Outline each blood parasite and name the species.
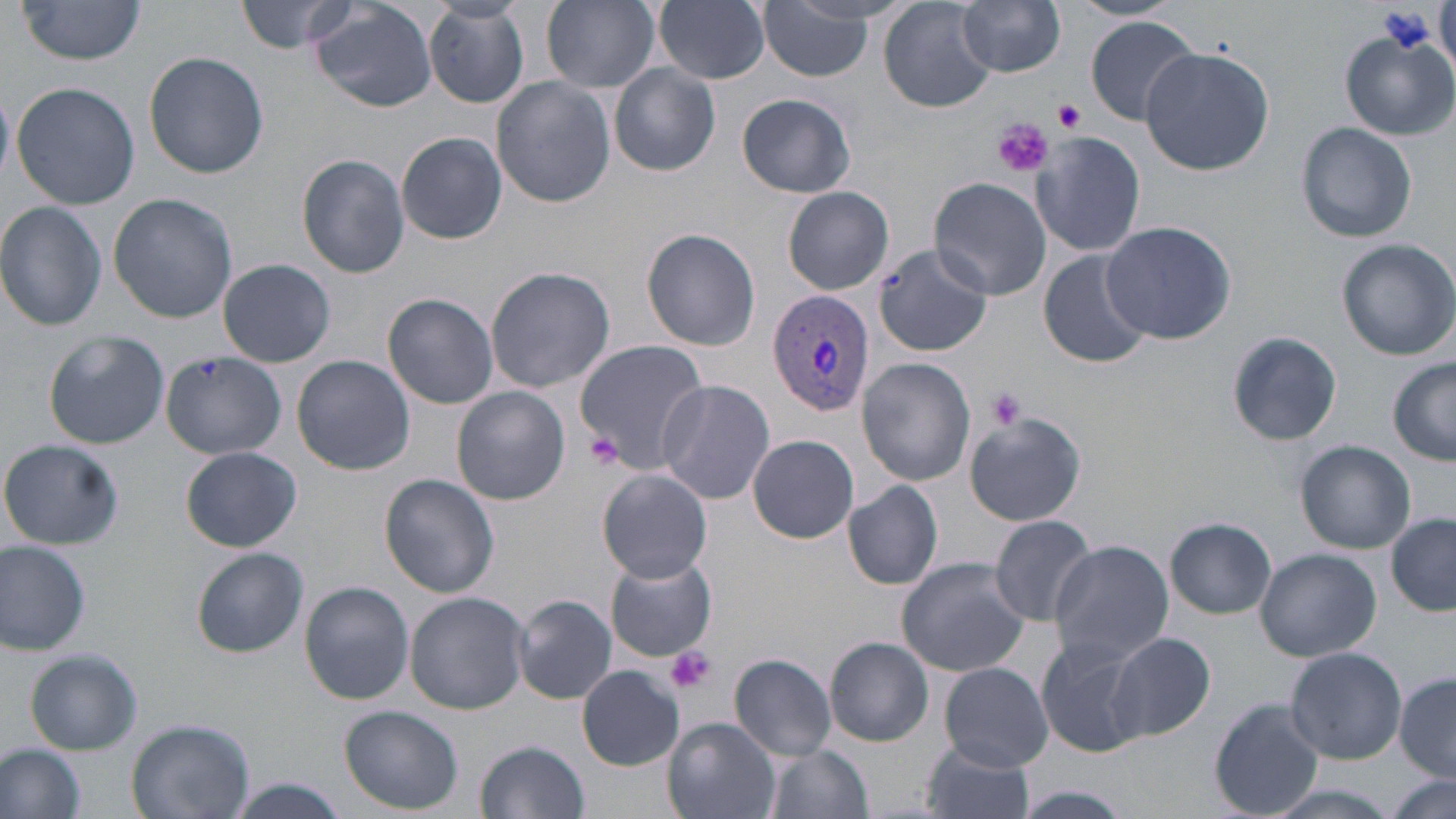

Approximate bounding boxes as [x1, y1, x2, y2] in pixels.
Plasmodium vivax-infected red blood cells: [768, 289, 875, 419].
No Plasmodium falciparum, Plasmodium ovale, Plasmodium malariae, Babesia divergens, or Trypanosoma brucei observed.

Platelet locations: [1054, 98, 1086, 132], [992, 118, 1052, 177], [985, 386, 1027, 429], [582, 432, 626, 468], [665, 646, 714, 694]. Uninfected red blood cell locations: [237, 0, 357, 54], [541, 0, 661, 91], [654, 0, 770, 85], [755, 0, 879, 82], [880, 0, 994, 113], [17, 1, 148, 67], [1069, 1, 1180, 22], [309, 2, 439, 112], [424, 2, 530, 110], [956, 2, 1066, 76], [1085, 16, 1201, 124], [1341, 33, 1456, 139], [1140, 44, 1277, 176], [144, 51, 269, 178], [608, 63, 721, 176], [491, 77, 618, 209], [12, 82, 141, 210], [737, 93, 856, 197], [1296, 121, 1417, 244], [396, 131, 507, 244], [1030, 131, 1146, 257], [296, 153, 410, 278], [929, 176, 1052, 301], [783, 186, 895, 294], [108, 192, 238, 322], [0, 201, 107, 331], [1100, 220, 1239, 345], [641, 228, 762, 351], [1336, 239, 1456, 360], [876, 241, 988, 356], [1037, 249, 1155, 369], [218, 258, 335, 368], [485, 266, 615, 394], [383, 293, 499, 409], [42, 329, 170, 450], [1225, 329, 1342, 446], [574, 339, 709, 467], [161, 349, 289, 460], [292, 355, 415, 476], [858, 358, 976, 485], [1388, 358, 1456, 466], [654, 379, 775, 504], [451, 386, 571, 506], [963, 411, 1086, 527], [747, 435, 860, 543], [1, 438, 124, 550], [1296, 440, 1417, 553], [181, 446, 301, 552], [595, 468, 714, 584], [380, 474, 501, 597], [843, 481, 943, 590], [1387, 513, 1456, 617], [987, 514, 1098, 626], [1166, 517, 1276, 618], [0, 540, 92, 657], [1047, 540, 1173, 666], [193, 547, 308, 657], [1254, 547, 1381, 661], [604, 555, 717, 662], [897, 557, 1030, 678], [299, 581, 414, 704], [405, 591, 530, 714], [512, 594, 617, 704], [1107, 631, 1217, 744], [1035, 636, 1149, 758], [825, 637, 934, 747], [1285, 647, 1407, 763], [25, 648, 143, 755], [730, 653, 837, 759], [938, 663, 1054, 771], [576, 666, 684, 770], [1396, 671, 1456, 778], [1209, 699, 1325, 817], [340, 706, 462, 814], [126, 717, 253, 819], [663, 718, 780, 819], [476, 739, 590, 818], [919, 739, 1036, 819], [0, 743, 87, 818], [762, 744, 873, 819], [1386, 773, 1452, 817], [227, 780, 350, 818], [999, 785, 1144, 819]. Slide-level diagnosis: Plasmodium vivax. May-Grünwald-Giemsa-stained preparation. Thin blood smear. Image is 1456×819 pixels. 1000x magnification. Optical microscopy. Single field of view.